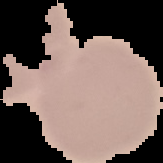

Summary:
  - Image type: segmented cell region on a black background
  - Preparation: thin blood smear
  - Image size: 163×163 pixels
  - Result: negative for Plasmodium parasites